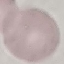
{
  "malaria_status": "uninfected",
  "preparation": "thin blood smear",
  "image_type": "automatically extracted cell patch, resized to 64 × 64 pixels",
  "stain": "Giemsa",
  "capture": "smartphone camera at the microscope eyepiece"
}